Report the malaria status of this cell.
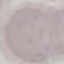
Uninfected.

{
  "stain": "Giemsa",
  "preparation": "thin blood smear",
  "image_type": "cell patch, automatically extracted from a larger field of view and resized to 64 × 64 pixels",
  "capture": "smartphone camera at the microscope eyepiece"
}